Assess the morphology of the erythrocytes.
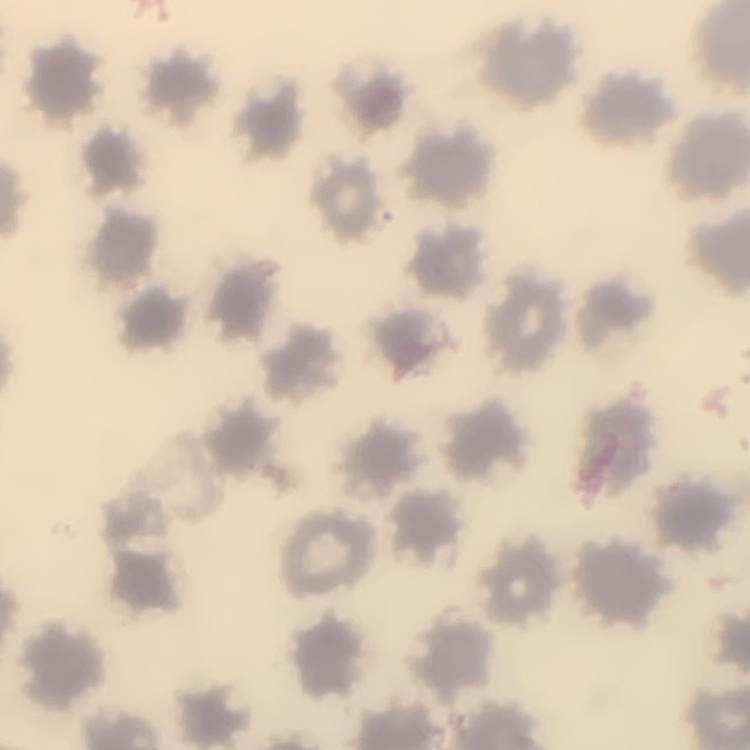

They show no rouleaux formation.

preparation: thin blood smear
stain: Field's or Giemsa
image_type: square crop of a larger photomicrograph